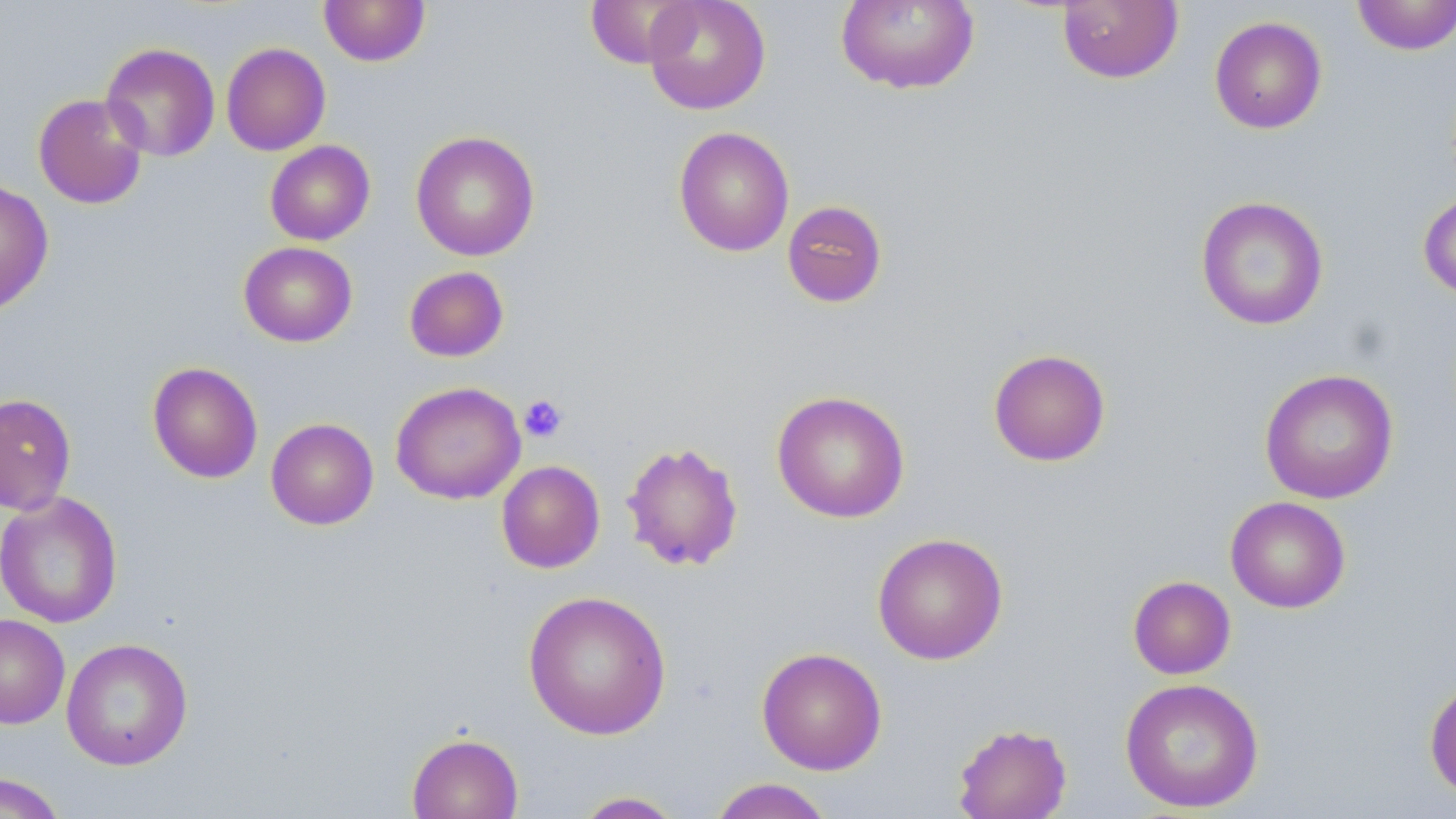
slide-level diagnosis = negative for blood parasites
uninfected red blood cell locations = approximate bounding boxes as named x1/y1/x2/y2 corners in pixels: (x1=318, y1=0, x2=431, y2=67), (x1=585, y1=0, x2=697, y2=69), (x1=643, y1=0, x2=771, y2=115), (x1=1351, y1=0, x2=1456, y2=56), (x1=836, y1=1, x2=979, y2=95), (x1=1056, y1=1, x2=1183, y2=84), (x1=1209, y1=15, x2=1328, y2=134), (x1=100, y1=42, x2=221, y2=163), (x1=221, y1=42, x2=331, y2=156), (x1=32, y1=93, x2=149, y2=209), (x1=673, y1=126, x2=795, y2=257), (x1=411, y1=130, x2=540, y2=261), (x1=265, y1=140, x2=375, y2=245), (x1=0, y1=179, x2=54, y2=316), (x1=1417, y1=189, x2=1456, y2=301), (x1=1196, y1=195, x2=1329, y2=331), (x1=782, y1=200, x2=888, y2=308), (x1=238, y1=241, x2=357, y2=347), (x1=403, y1=266, x2=509, y2=362), (x1=987, y1=348, x2=1111, y2=466), (x1=147, y1=361, x2=264, y2=484), (x1=1259, y1=368, x2=1399, y2=504), (x1=390, y1=381, x2=526, y2=505), (x1=771, y1=390, x2=910, y2=523), (x1=0, y1=393, x2=76, y2=516), (x1=265, y1=418, x2=379, y2=530), (x1=621, y1=440, x2=745, y2=572), (x1=496, y1=460, x2=605, y2=573), (x1=0, y1=492, x2=123, y2=628), (x1=1225, y1=496, x2=1351, y2=614), (x1=871, y1=532, x2=1009, y2=665), (x1=1128, y1=575, x2=1236, y2=679), (x1=522, y1=590, x2=672, y2=740), (x1=0, y1=614, x2=70, y2=729), (x1=60, y1=638, x2=194, y2=770), (x1=756, y1=646, x2=888, y2=775), (x1=1119, y1=677, x2=1265, y2=813), (x1=1424, y1=678, x2=1456, y2=803), (x1=952, y1=722, x2=1073, y2=819), (x1=406, y1=732, x2=524, y2=819), (x1=0, y1=772, x2=67, y2=819), (x1=708, y1=778, x2=836, y2=819), (x1=572, y1=791, x2=686, y2=818)
field of view = one of a larger specimen
modality = optical microscopy
preparation = thin blood film
stain = May-Grünwald-Giemsa
magnification = 1000x
image size = 1456×819 pixels
platelet locations = approximate bounding boxes as named x1/y1/x2/y2 corners in pixels: (x1=519, y1=394, x2=568, y2=443)